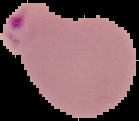
Image is 139×121 pixels. Cell region segmented out of the field of view; the surrounding area is masked to black. From a thin blood film. Malaria status: parasitized.